Outline each Plasmodium falciparum-infected red blood cell.
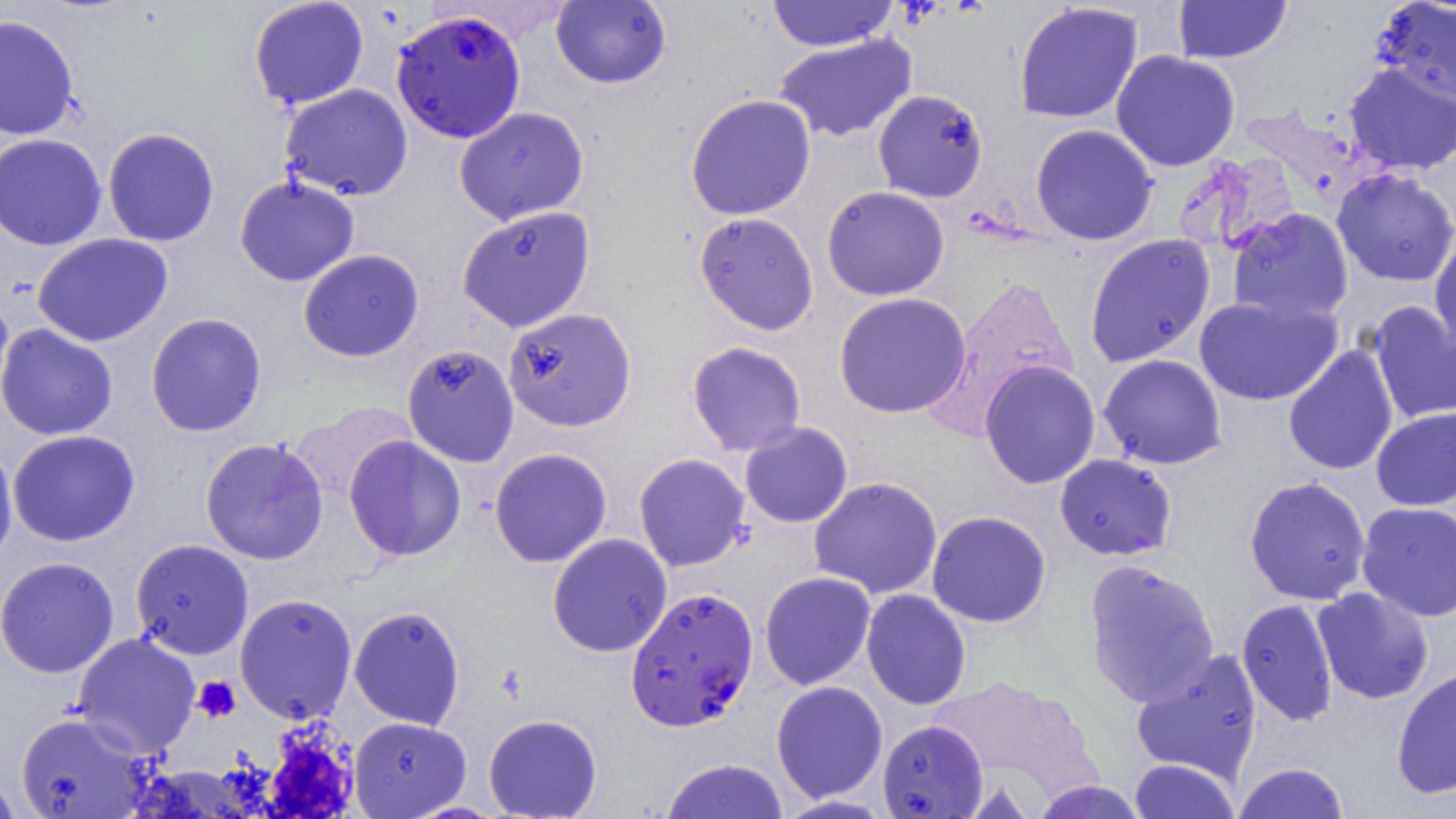

Approximate bounding boxes as [x1, y1, x2, y2] in pixels.
Plasmodium falciparum-infected red blood cells: [391, 8, 526, 143], [624, 587, 759, 731].

Platelet locations: [192, 675, 241, 723], [261, 725, 359, 817]. Uninfected red blood cell locations: [766, 0, 897, 51], [1172, 0, 1292, 63], [248, 1, 369, 109], [551, 1, 672, 89], [1370, 1, 1456, 106], [1013, 3, 1143, 125], [0, 14, 80, 141], [774, 33, 917, 143], [1110, 50, 1241, 172], [1343, 63, 1456, 176], [279, 84, 413, 201], [872, 89, 988, 203], [685, 93, 816, 221], [454, 106, 589, 225], [1030, 124, 1159, 246], [102, 127, 219, 246], [0, 133, 107, 250], [1175, 152, 1303, 257], [1331, 168, 1456, 287], [234, 175, 359, 286], [821, 186, 950, 301], [457, 205, 596, 333], [1226, 207, 1354, 324], [694, 212, 819, 336], [1429, 232, 1456, 357], [32, 233, 173, 346], [1084, 233, 1216, 367], [298, 249, 424, 362], [926, 274, 1079, 435], [0, 291, 14, 409], [833, 292, 971, 418], [1194, 294, 1343, 407], [1367, 301, 1456, 425], [497, 306, 629, 432], [145, 312, 268, 437], [0, 323, 118, 441], [687, 341, 807, 456], [402, 343, 519, 467], [1283, 345, 1399, 476], [1098, 354, 1227, 470], [979, 360, 1101, 489], [288, 401, 416, 505], [1371, 407, 1456, 511], [739, 421, 853, 528], [7, 429, 140, 547], [343, 435, 467, 562], [200, 437, 328, 565], [0, 441, 18, 568], [489, 447, 612, 568], [633, 453, 751, 572], [1054, 453, 1178, 561], [808, 476, 943, 599], [1244, 476, 1372, 605], [1356, 502, 1456, 622], [926, 510, 1052, 628], [547, 533, 672, 657], [130, 539, 254, 660], [0, 556, 119, 678], [1083, 559, 1220, 707], [759, 571, 876, 690], [1312, 587, 1434, 704], [861, 589, 971, 710], [234, 593, 357, 724], [1236, 598, 1339, 727], [349, 606, 465, 730], [72, 632, 201, 758], [1131, 648, 1263, 784], [1391, 666, 1456, 800], [927, 676, 1095, 793], [771, 680, 888, 803], [15, 711, 153, 818], [483, 713, 603, 818], [349, 716, 470, 818], [877, 720, 988, 818], [659, 758, 788, 819], [1128, 759, 1241, 818], [1233, 762, 1350, 819], [0, 769, 22, 819], [1029, 780, 1150, 819], [774, 795, 894, 818]. Slide-level diagnosis: Plasmodium falciparum. Thin blood film. One field of a larger specimen. Image is 1456×819 pixels. 1000x magnification. Light microscopy.